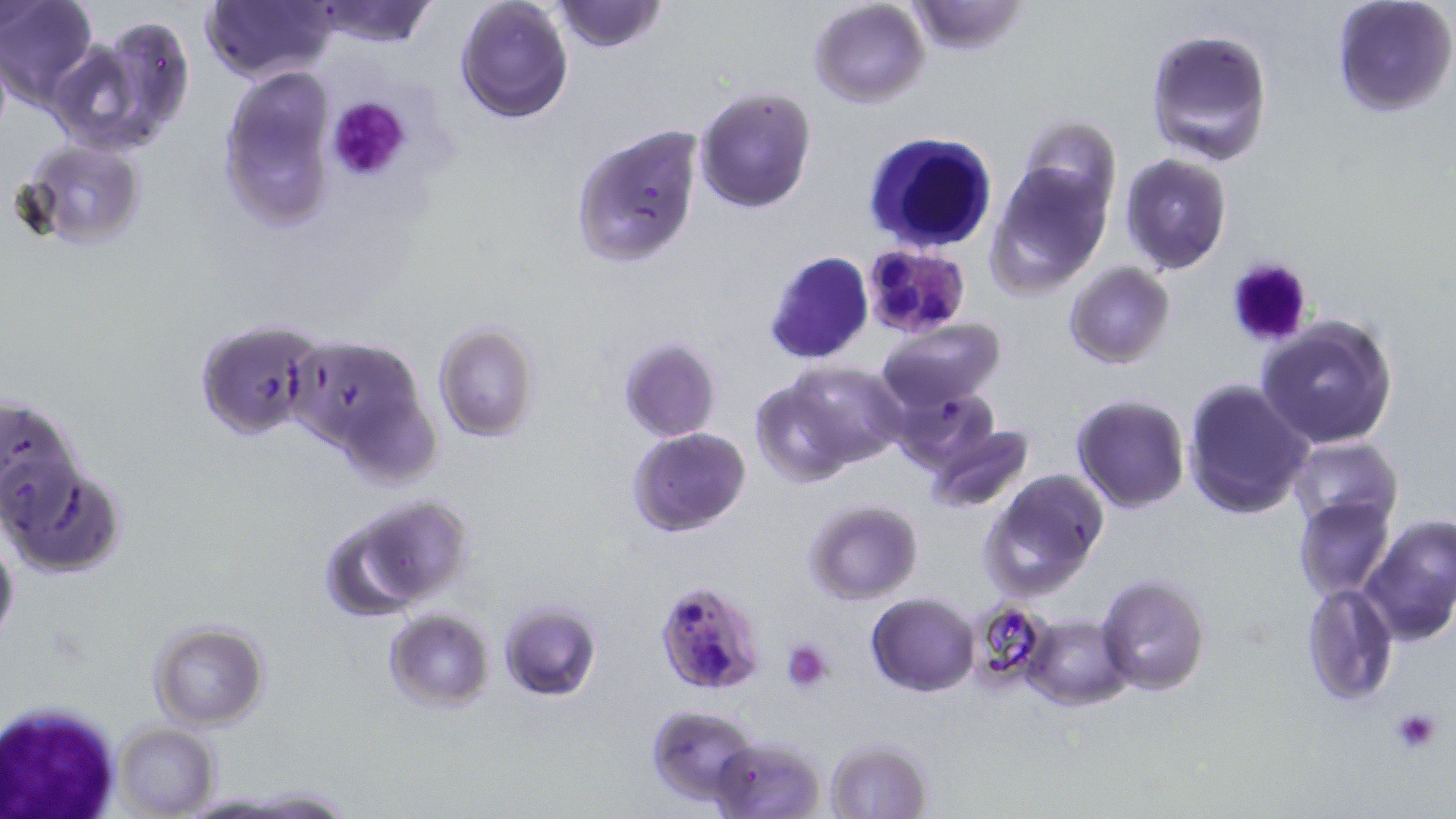

slide-level diagnosis = Plasmodium falciparum
modality = optical microscopy
magnification = 1000x
Plasmodium falciparum-infected red blood cell locations = approximate bounding boxes as named x1/y1/x2/y2 corners in pixels: (x1=864, y1=243, x2=973, y2=333), (x1=655, y1=579, x2=766, y2=693)
white blood cell locations = approximate bounding boxes as named x1/y1/x2/y2 corners in pixels: (x1=865, y1=132, x2=998, y2=254), (x1=1, y1=698, x2=125, y2=818)
image size = 1456×819 pixels
preparation = thin blood smear
uninfected red blood cell locations = approximate bounding boxes as named x1/y1/x2/y2 corners in pixels: (x1=1, y1=0, x2=98, y2=107), (x1=202, y1=0, x2=336, y2=84), (x1=305, y1=0, x2=438, y2=48), (x1=455, y1=0, x2=575, y2=124), (x1=553, y1=0, x2=668, y2=53), (x1=905, y1=0, x2=1028, y2=54), (x1=1330, y1=0, x2=1455, y2=119), (x1=808, y1=1, x2=931, y2=108), (x1=49, y1=17, x2=193, y2=157), (x1=1144, y1=28, x2=1274, y2=165), (x1=0, y1=41, x2=12, y2=144), (x1=219, y1=68, x2=338, y2=229), (x1=693, y1=88, x2=815, y2=212), (x1=1017, y1=116, x2=1121, y2=220), (x1=569, y1=124, x2=704, y2=267), (x1=18, y1=140, x2=148, y2=251), (x1=1119, y1=154, x2=1233, y2=274), (x1=985, y1=165, x2=1112, y2=298), (x1=763, y1=251, x2=872, y2=364), (x1=1064, y1=261, x2=1176, y2=369), (x1=1256, y1=315, x2=1399, y2=450), (x1=194, y1=318, x2=325, y2=441), (x1=877, y1=319, x2=1007, y2=411), (x1=432, y1=322, x2=539, y2=442), (x1=285, y1=334, x2=437, y2=472), (x1=618, y1=338, x2=721, y2=442), (x1=779, y1=361, x2=907, y2=468), (x1=1183, y1=378, x2=1314, y2=521), (x1=750, y1=381, x2=861, y2=487), (x1=887, y1=383, x2=1001, y2=472), (x1=0, y1=394, x2=84, y2=527), (x1=1072, y1=394, x2=1191, y2=512), (x1=923, y1=424, x2=1034, y2=514), (x1=627, y1=426, x2=751, y2=536), (x1=1288, y1=438, x2=1402, y2=531), (x1=4, y1=464, x2=127, y2=576), (x1=979, y1=471, x2=1108, y2=602), (x1=347, y1=495, x2=476, y2=607), (x1=1292, y1=496, x2=1394, y2=601), (x1=804, y1=500, x2=923, y2=604), (x1=1360, y1=514, x2=1456, y2=646), (x1=0, y1=534, x2=20, y2=645), (x1=1096, y1=574, x2=1210, y2=696), (x1=1300, y1=580, x2=1398, y2=707), (x1=867, y1=592, x2=979, y2=695), (x1=498, y1=600, x2=601, y2=701), (x1=384, y1=610, x2=494, y2=711), (x1=1022, y1=615, x2=1135, y2=710), (x1=148, y1=620, x2=270, y2=730), (x1=647, y1=703, x2=763, y2=807), (x1=112, y1=721, x2=221, y2=819), (x1=710, y1=735, x2=827, y2=818), (x1=823, y1=738, x2=935, y2=819)
platelet locations = approximate bounding boxes as named x1/y1/x2/y2 corners in pixels: (x1=326, y1=94, x2=413, y2=185), (x1=1226, y1=258, x2=1317, y2=349), (x1=781, y1=640, x2=834, y2=691), (x1=1389, y1=706, x2=1444, y2=755)
stain = May-Grünwald-Giemsa
field of view = single